Locate every Plasmodium falciparum-infected red blood cell.
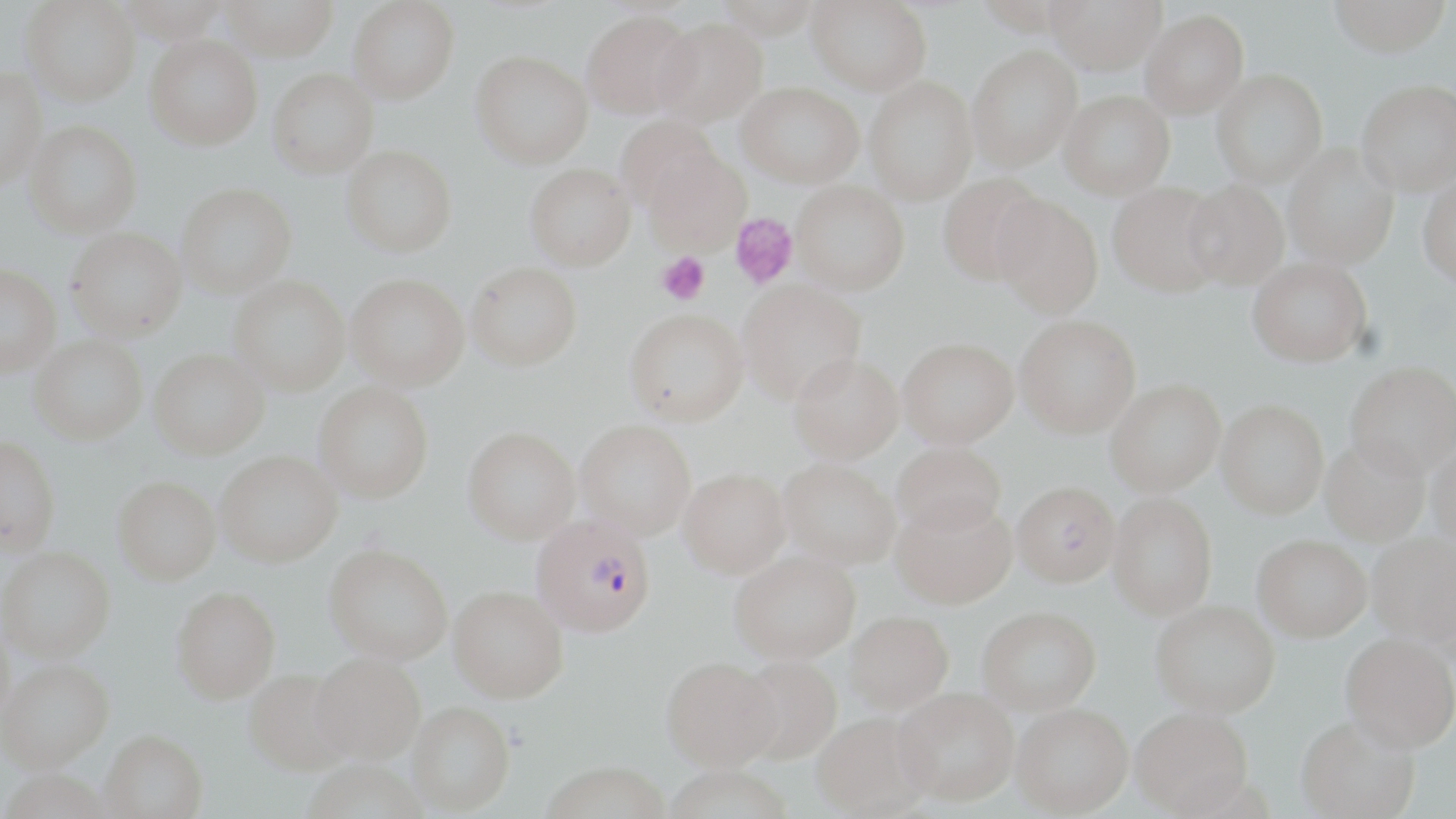

Approximate bounding boxes as (x1, y1, x2, y2) in pixels.
Plasmodium falciparum-infected red blood cells: (531, 515, 656, 636).

Uninfected red blood cell locations: (217, 0, 339, 61), (712, 0, 823, 39), (806, 0, 932, 96), (1044, 0, 1165, 74), (1327, 0, 1451, 57), (21, 1, 141, 105), (347, 1, 460, 104), (581, 9, 698, 119), (1140, 9, 1249, 118), (653, 17, 768, 126), (145, 34, 262, 150), (967, 45, 1082, 172), (470, 49, 593, 169), (0, 65, 46, 190), (1211, 68, 1327, 187), (267, 69, 378, 178), (864, 76, 978, 206), (1357, 78, 1456, 196), (737, 81, 864, 188), (1059, 90, 1174, 199), (616, 115, 722, 212), (25, 121, 143, 238), (341, 144, 457, 256), (1283, 144, 1399, 269), (644, 150, 752, 256), (525, 162, 636, 270), (938, 172, 1049, 285), (1418, 176, 1456, 287), (1182, 179, 1289, 290), (791, 180, 909, 295), (1107, 182, 1226, 297), (176, 183, 296, 298), (991, 194, 1104, 318), (66, 227, 186, 341), (1248, 256, 1372, 366), (466, 261, 582, 371), (0, 264, 60, 377), (346, 274, 470, 390), (229, 275, 350, 395), (737, 279, 866, 404), (624, 307, 749, 426), (1015, 315, 1140, 438), (30, 336, 147, 444), (898, 337, 1018, 447), (149, 349, 269, 459), (789, 353, 903, 463), (1345, 361, 1456, 477), (1105, 379, 1225, 497), (314, 382, 434, 502), (1216, 399, 1329, 518), (575, 419, 696, 539), (463, 426, 580, 544), (0, 435, 61, 554), (1320, 437, 1430, 546), (892, 442, 1006, 536), (1427, 442, 1456, 549), (215, 450, 342, 566), (778, 458, 900, 569), (678, 468, 790, 578), (113, 475, 221, 585), (1011, 480, 1119, 587), (1108, 492, 1218, 621), (891, 496, 1017, 609), (1367, 532, 1456, 649), (1252, 533, 1372, 641), (324, 543, 453, 664), (0, 546, 114, 662), (731, 550, 860, 663), (448, 584, 569, 702), (171, 585, 281, 703), (1151, 600, 1279, 717), (977, 605, 1101, 714), (845, 610, 953, 713), (0, 619, 15, 728), (1341, 633, 1456, 752), (309, 651, 426, 764), (736, 656, 842, 765), (0, 657, 114, 772), (662, 657, 781, 771), (244, 668, 354, 775), (894, 687, 1018, 806), (408, 702, 515, 814), (1011, 703, 1133, 816), (1132, 707, 1254, 816), (812, 711, 932, 818), (1296, 714, 1419, 818), (100, 729, 208, 819), (541, 761, 671, 819), (663, 765, 794, 819). Platelet locations: (729, 214, 798, 289), (656, 252, 710, 305). Slide-level diagnosis: Plasmodium falciparum. May-Grünwald-Giemsa-stained preparation. Image is 1456×819 pixels. 1000x magnification. One field of a larger specimen. Thin blood film. Light microscopy.